Name the blood parasite species.
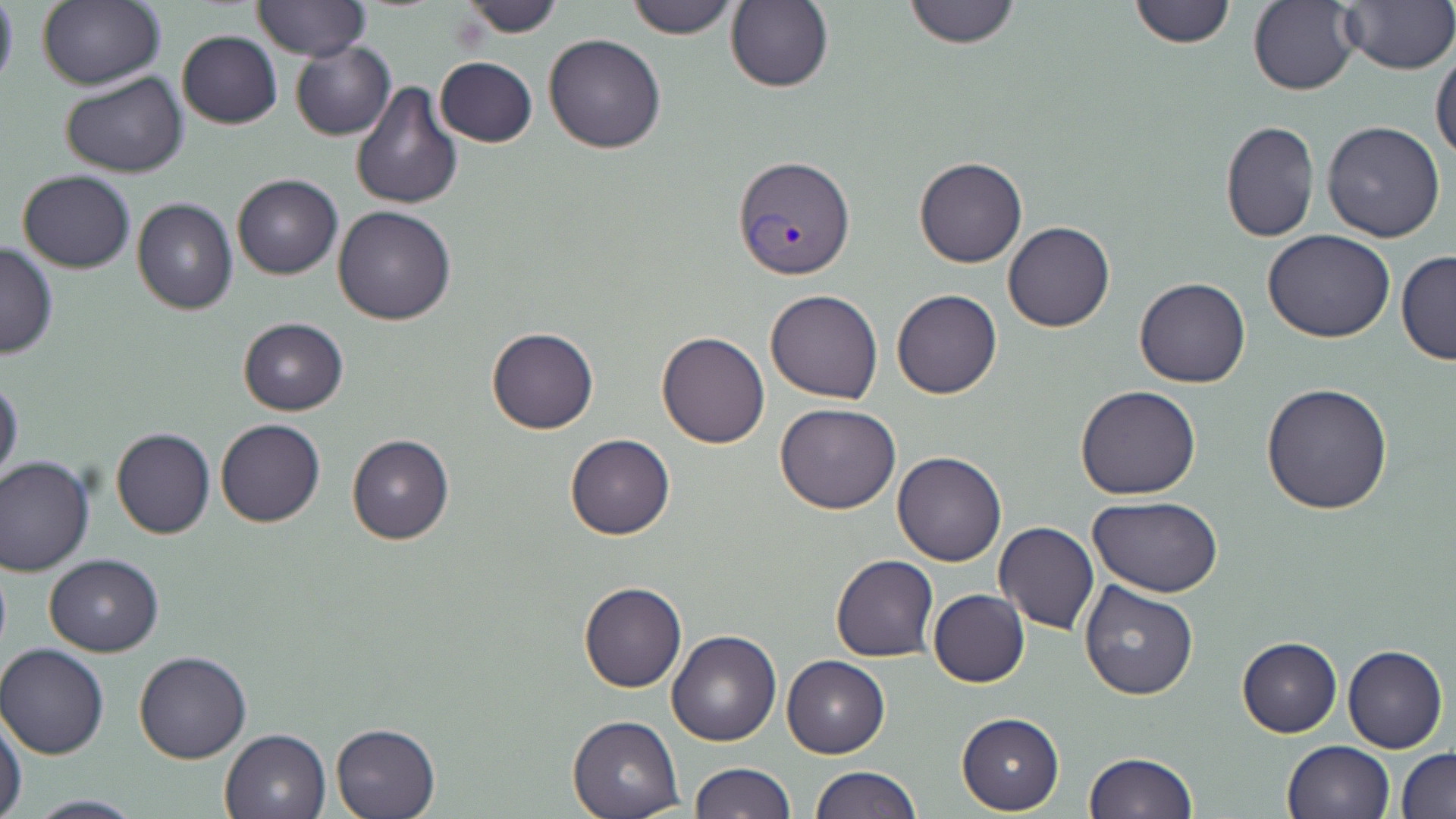
Plasmodium vivax.

{
  "magnification": "1000x",
  "stain": "May-Grünwald-Giemsa",
  "plasmodium_vivax_infected_red_blood_cell_locations": "approximate bounding boxes as [x1, y1, x2, y2] in pixels: [731, 154, 853, 280]",
  "field_of_view": "single",
  "modality": "optical microscopy",
  "preparation": "thin blood film",
  "image_size": "1456×819 pixels",
  "uninfected_red_blood_cell_locations": "approximate bounding boxes as [x1, y1, x2, y2] in pixels: [0, 0, 19, 95], [37, 0, 165, 90], [255, 0, 368, 60], [458, 0, 566, 38], [625, 0, 741, 37], [902, 0, 1020, 48], [1127, 0, 1236, 47], [1248, 1, 1361, 96], [725, 2, 833, 92], [1337, 2, 1456, 76], [177, 31, 282, 128], [543, 33, 667, 153], [290, 41, 396, 140], [1431, 47, 1456, 165], [434, 57, 537, 148], [60, 71, 187, 178], [351, 79, 465, 211], [1219, 119, 1319, 244], [1321, 120, 1446, 242], [914, 156, 1027, 267], [17, 171, 136, 273], [231, 174, 342, 280], [132, 198, 238, 315], [333, 206, 456, 326], [1003, 222, 1114, 332], [1263, 230, 1395, 344], [0, 241, 58, 358], [1396, 250, 1456, 366], [1134, 276, 1250, 388], [765, 289, 884, 403], [892, 289, 1002, 399], [238, 318, 349, 415], [485, 327, 598, 434], [657, 331, 769, 449], [0, 376, 23, 487], [1261, 382, 1394, 516], [1074, 384, 1201, 499], [774, 403, 902, 514], [215, 418, 325, 527], [110, 427, 215, 539], [345, 433, 453, 545], [565, 433, 675, 539], [893, 452, 1007, 566], [0, 456, 95, 575], [1088, 496, 1223, 597], [994, 523, 1099, 635], [43, 554, 165, 655], [831, 554, 938, 662], [1078, 578, 1199, 700], [578, 581, 686, 693], [928, 590, 1029, 687], [667, 630, 781, 746], [1237, 636, 1342, 738], [0, 643, 109, 759], [1343, 644, 1448, 754], [134, 651, 252, 763], [782, 655, 888, 759], [956, 712, 1064, 814], [568, 713, 684, 817], [0, 716, 27, 819], [330, 722, 439, 818], [219, 728, 331, 818], [1282, 740, 1396, 819], [1397, 748, 1456, 819], [1084, 750, 1197, 818], [686, 761, 794, 818], [808, 766, 922, 819], [18, 794, 148, 819]"
}